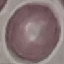

Summary:
  - Malaria status: uninfected
  - Capture: smartphone through the microscope eyepiece
  - Preparation: thin blood film
  - Stain: Giemsa
  - Image type: cell patch, automatically extracted from a larger field of view and resized to 64 × 64 pixels